State the blood parasite species.
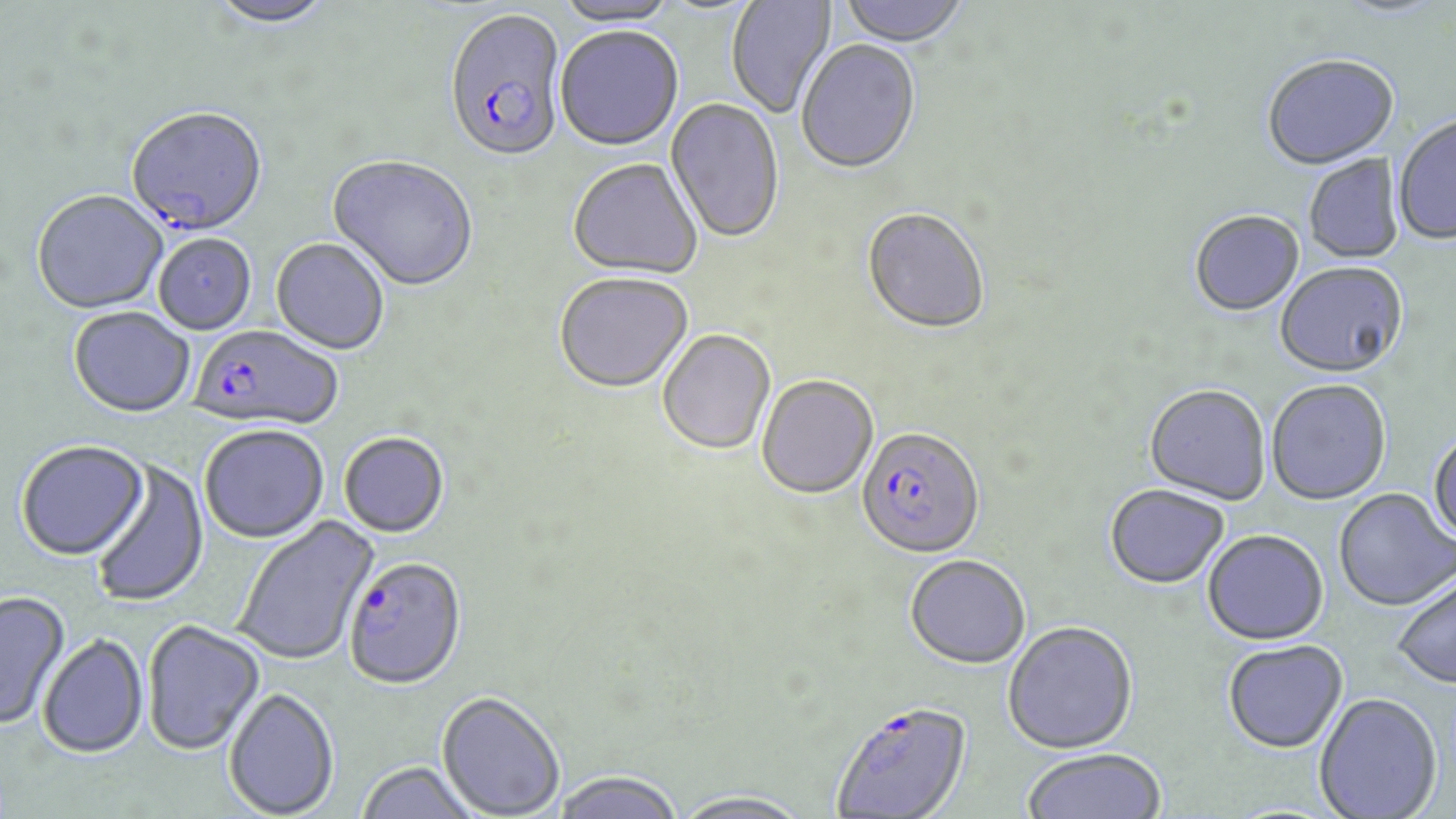
Plasmodium falciparum.

Summary:
  - Coordinate format: approximate bounding boxes as named x1/y1/x2/y2 corners in pixels
  - Uninfected red blood cell locations: (x1=206, y1=0, x2=338, y2=30), (x1=555, y1=0, x2=680, y2=30), (x1=727, y1=0, x2=837, y2=119), (x1=837, y1=0, x2=971, y2=50), (x1=554, y1=29, x2=683, y2=154), (x1=796, y1=42, x2=921, y2=176), (x1=1262, y1=56, x2=1399, y2=172), (x1=665, y1=98, x2=785, y2=246), (x1=1393, y1=116, x2=1456, y2=247), (x1=1304, y1=154, x2=1405, y2=264), (x1=328, y1=157, x2=479, y2=293), (x1=567, y1=161, x2=702, y2=282), (x1=31, y1=192, x2=167, y2=315), (x1=862, y1=209, x2=990, y2=336), (x1=1189, y1=211, x2=1305, y2=318), (x1=154, y1=235, x2=257, y2=335), (x1=270, y1=239, x2=389, y2=356), (x1=1275, y1=265, x2=1408, y2=381), (x1=555, y1=274, x2=694, y2=396), (x1=69, y1=308, x2=195, y2=419), (x1=658, y1=331, x2=776, y2=457), (x1=756, y1=376, x2=878, y2=502), (x1=1266, y1=381, x2=1391, y2=506), (x1=1144, y1=386, x2=1270, y2=506), (x1=199, y1=426, x2=330, y2=544), (x1=1427, y1=429, x2=1456, y2=546), (x1=339, y1=433, x2=450, y2=541), (x1=15, y1=442, x2=149, y2=562), (x1=90, y1=459, x2=209, y2=608), (x1=1104, y1=485, x2=1229, y2=590), (x1=1334, y1=488, x2=1455, y2=611), (x1=233, y1=515, x2=379, y2=667), (x1=1202, y1=530, x2=1328, y2=646), (x1=905, y1=555, x2=1031, y2=669), (x1=1392, y1=573, x2=1456, y2=690), (x1=0, y1=591, x2=70, y2=729), (x1=142, y1=620, x2=265, y2=756), (x1=1003, y1=622, x2=1138, y2=754), (x1=37, y1=634, x2=149, y2=759), (x1=1222, y1=640, x2=1348, y2=753), (x1=224, y1=688, x2=339, y2=818), (x1=1314, y1=692, x2=1442, y2=819), (x1=436, y1=693, x2=565, y2=818), (x1=1021, y1=748, x2=1167, y2=819), (x1=356, y1=762, x2=481, y2=819), (x1=551, y1=771, x2=684, y2=819), (x1=670, y1=789, x2=815, y2=819)
  - Plasmodium falciparum-infected red blood cell locations: (x1=443, y1=12, x2=568, y2=166), (x1=126, y1=110, x2=268, y2=239), (x1=187, y1=326, x2=343, y2=432), (x1=856, y1=428, x2=985, y2=560), (x1=342, y1=559, x2=468, y2=692), (x1=830, y1=700, x2=972, y2=818)
  - Field of view: single
  - Preparation: thin blood smear
  - Image size: 1456×819 pixels
  - Magnification: 1000x
  - Stain: May-Grünwald-Giemsa
  - Modality: optical microscopy